Assess the morphology of the erythrocytes.
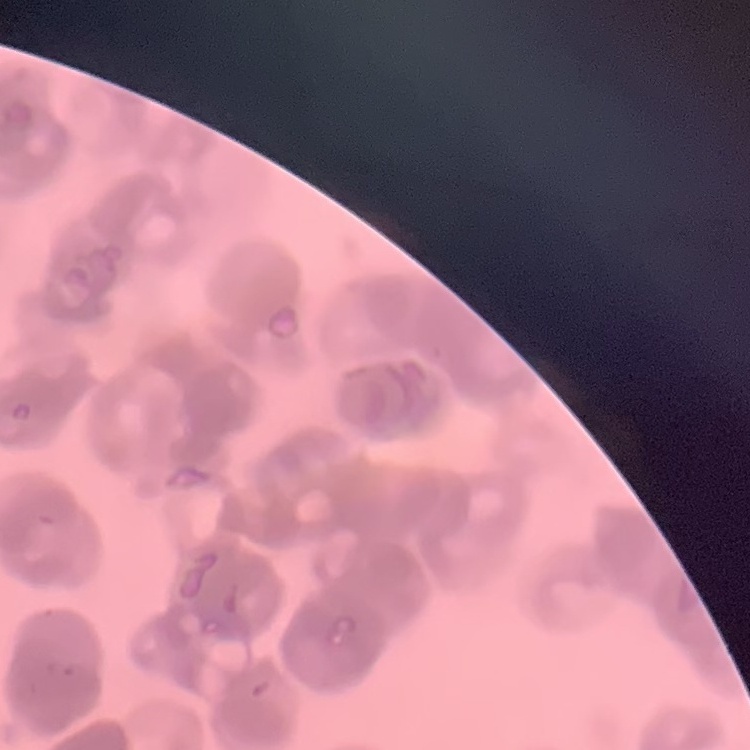

They show rouleaux formation.

{
  "preparation": "thin peripheral smear",
  "stain": "Field's or Giemsa",
  "image_type": "one tile cut from a larger photomicrograph"
}